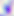

Summary:
  - Identification: Toxoplasma gondii
  - Modality: micrograph
  - Magnification: 400x